State which parasite is depicted.
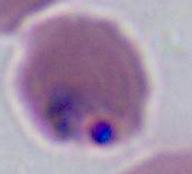

Plasmodium.

magnification = 400x or 1000x
modality = photomicrograph